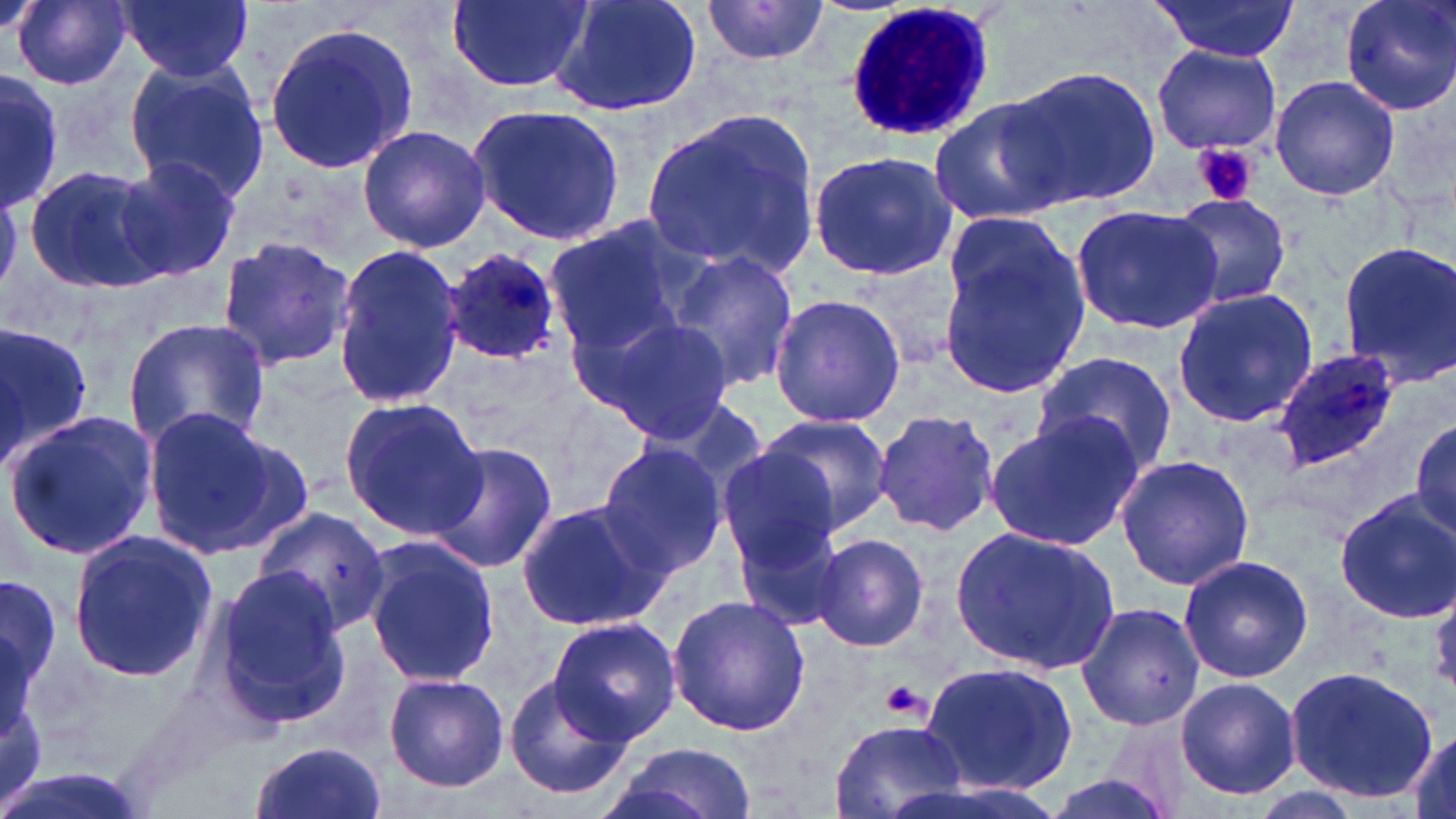

Summary:
  - Coordinate format: approximate bounding boxes as [x1, y1, x2, y2] in pixels
  - Platelet locations: [1192, 142, 1260, 207], [881, 680, 928, 720]
  - Plasmodium ovale-infected red blood cell locations: [442, 249, 564, 363], [1272, 349, 1403, 472]
  - Uninfected red blood cell locations: [13, 0, 133, 90], [118, 0, 253, 82], [447, 0, 592, 92], [544, 0, 702, 118], [1148, 0, 1301, 62], [1338, 0, 1456, 115], [700, 1, 830, 66], [262, 17, 423, 175], [1152, 43, 1281, 155], [121, 57, 268, 205], [1006, 67, 1161, 210], [1, 71, 62, 210], [1270, 75, 1400, 203], [929, 96, 1070, 223], [468, 102, 626, 247], [640, 105, 823, 283], [357, 124, 491, 252], [806, 151, 959, 283], [113, 157, 240, 280], [23, 163, 172, 295], [1168, 192, 1293, 309], [1069, 203, 1222, 335], [540, 218, 694, 354], [935, 224, 1092, 402], [214, 235, 358, 371], [1337, 240, 1456, 385], [330, 243, 466, 408], [666, 248, 800, 395], [856, 256, 965, 364], [1171, 287, 1318, 428], [768, 294, 907, 429], [575, 311, 731, 443], [123, 317, 270, 453], [0, 320, 96, 467], [1031, 352, 1177, 479], [338, 397, 486, 542], [143, 407, 313, 560], [4, 408, 160, 562], [871, 410, 1002, 538], [985, 411, 1143, 550], [757, 414, 894, 534], [1411, 418, 1455, 538], [425, 440, 557, 575], [595, 441, 730, 579], [716, 447, 842, 571], [1115, 455, 1255, 592], [1334, 490, 1456, 622], [516, 497, 670, 634], [255, 506, 389, 636], [729, 517, 849, 636], [951, 527, 1118, 672], [67, 530, 216, 683], [809, 534, 932, 652], [362, 537, 503, 689], [1177, 554, 1314, 683], [209, 568, 349, 729], [0, 570, 64, 708], [1428, 586, 1456, 696], [667, 595, 811, 737], [1075, 603, 1204, 731], [548, 616, 682, 743], [920, 660, 1079, 794], [1285, 664, 1437, 801], [504, 671, 634, 799], [382, 672, 510, 791], [1173, 677, 1304, 801], [828, 716, 969, 819], [1404, 727, 1456, 819], [248, 741, 388, 819], [607, 743, 757, 819]
  - White blood cell locations: [842, 2, 993, 144]
  - Slide-level diagnosis: Plasmodium ovale
  - Stain: May-Grünwald-Giemsa
  - Magnification: 1000x
  - Field of view: single
  - Image size: 1456×819 pixels
  - Modality: light microscopy
  - Preparation: thin blood smear